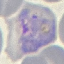
Result: malaria parasites identified. Giemsa-stained preparation. Thin blood smear. Automatically extracted cell patch, resized to 64 × 64 pixels. Acquired by smartphone through the microscope eyepiece.